Draw a bounding box around every leukocyte (white blood cell).
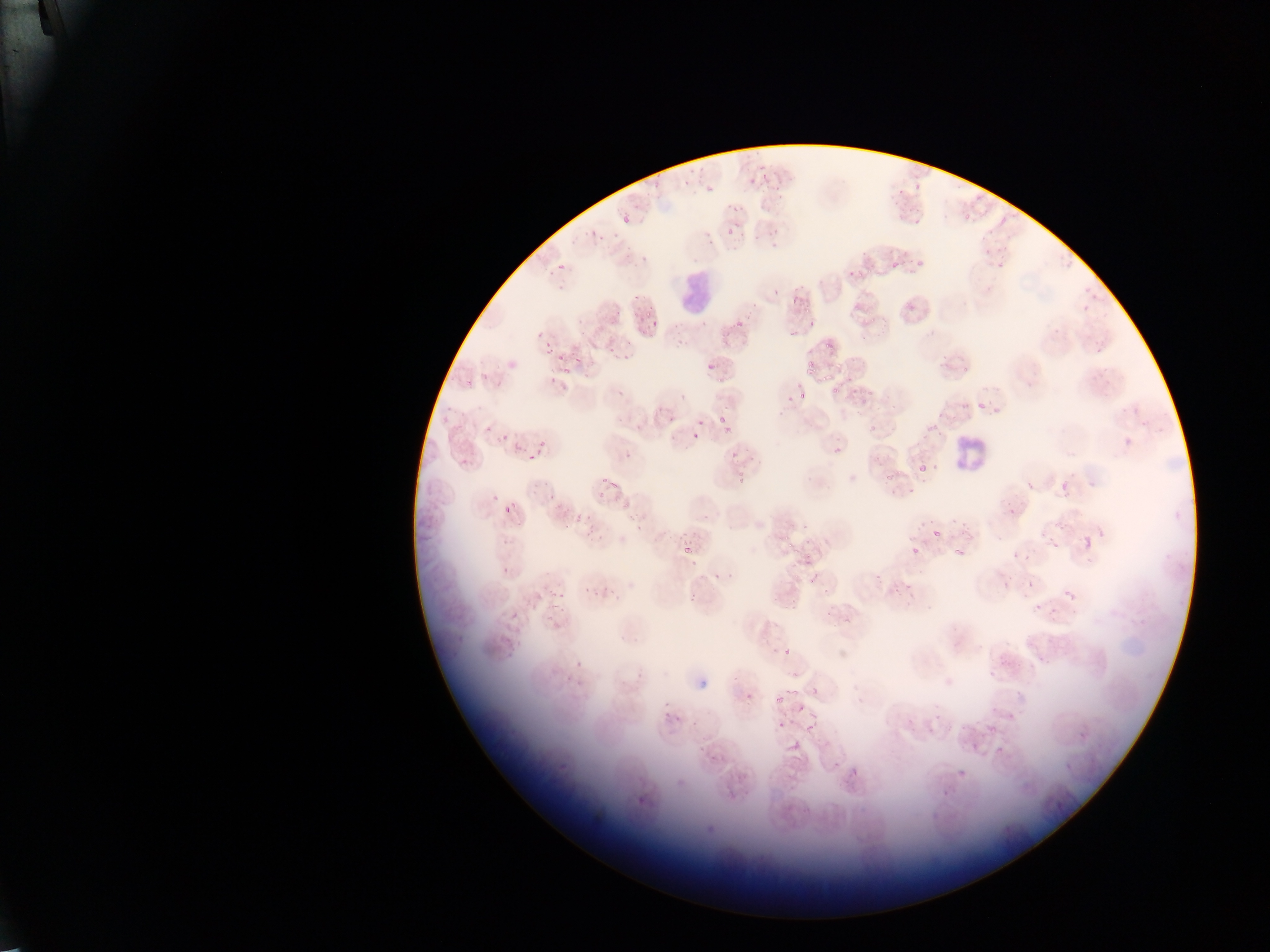

Approximate bounding boxes as [left, top, right, bottom] in pixels.
Leukocytes: [673, 266, 714, 311], [950, 440, 987, 471].

Plasmodium parasite locations = approximate bounding boxes as [left, top, right, bottom] in pixels: [656, 168, 662, 176], [763, 170, 768, 180], [749, 174, 758, 185], [684, 175, 692, 187], [913, 183, 922, 191], [772, 184, 780, 193], [732, 204, 740, 212], [622, 210, 636, 223], [962, 213, 972, 223], [591, 227, 598, 235], [726, 227, 734, 237], [769, 227, 782, 238], [569, 233, 577, 244], [889, 260, 901, 272], [557, 262, 568, 269], [547, 268, 556, 278], [856, 273, 864, 278], [557, 284, 564, 292], [771, 288, 781, 297], [789, 297, 799, 303], [802, 309, 810, 315], [645, 310, 651, 319], [807, 318, 820, 329], [650, 320, 657, 328], [734, 321, 746, 331], [578, 329, 587, 337], [789, 331, 797, 341], [537, 332, 545, 341], [544, 341, 553, 350], [826, 343, 833, 351], [543, 351, 551, 355], [622, 351, 628, 359], [571, 353, 582, 362], [557, 354, 565, 362], [706, 362, 715, 371], [805, 368, 813, 376], [822, 373, 833, 383], [465, 378, 471, 386], [618, 385, 629, 396], [830, 385, 841, 396], [784, 394, 794, 405], [977, 403, 986, 410], [1120, 409, 1128, 415], [717, 416, 725, 424], [1142, 420, 1148, 428], [483, 423, 494, 435], [870, 423, 878, 432], [723, 424, 732, 435], [501, 434, 512, 445], [692, 434, 698, 442], [1122, 435, 1133, 443], [536, 444, 544, 452], [623, 447, 631, 462], [730, 448, 741, 459], [526, 453, 535, 459], [460, 456, 472, 469], [934, 462, 938, 473], [919, 464, 929, 474], [601, 472, 609, 485], [737, 472, 745, 483], [884, 472, 894, 480], [607, 480, 619, 490], [1059, 480, 1069, 491], [1084, 481, 1092, 489], [1025, 482, 1032, 490], [908, 487, 916, 494], [546, 492, 554, 500], [593, 494, 603, 501], [511, 500, 517, 508], [622, 500, 632, 510], [502, 506, 510, 514], [1007, 507, 1015, 515], [703, 510, 711, 522], [574, 514, 581, 522], [949, 516, 957, 523], [927, 517, 937, 525], [961, 519, 969, 526], [634, 525, 643, 532], [960, 527, 968, 535], [932, 529, 941, 539], [584, 530, 595, 539], [675, 532, 687, 539], [995, 534, 1003, 541], [1079, 535, 1096, 555], [1049, 538, 1062, 552], [786, 539, 793, 550], [682, 542, 694, 554], [952, 545, 968, 562], [910, 546, 920, 556], [689, 559, 699, 567], [502, 562, 514, 575], [713, 570, 721, 584], [726, 572, 734, 580], [808, 574, 820, 586], [903, 580, 916, 588], [1026, 580, 1035, 590], [603, 584, 608, 592], [584, 586, 590, 594], [1062, 587, 1078, 604], [551, 589, 557, 599], [555, 592, 564, 601], [688, 592, 695, 602], [547, 599, 558, 610], [557, 608, 568, 618], [511, 611, 521, 621], [505, 635, 513, 642], [782, 647, 794, 656], [574, 663, 581, 671], [988, 668, 999, 676], [636, 672, 643, 680], [564, 674, 572, 682], [734, 674, 742, 683], [790, 687, 799, 696], [812, 688, 821, 696], [745, 691, 758, 703], [775, 695, 783, 703], [661, 700, 671, 708], [672, 716, 683, 724], [776, 718, 786, 726], [988, 720, 1000, 731], [803, 722, 813, 730], [970, 741, 978, 750], [699, 744, 708, 753], [993, 744, 1005, 754], [709, 753, 719, 765], [1063, 760, 1076, 774], [957, 763, 971, 776], [938, 788, 950, 796], [1054, 798, 1068, 814] | approximate [x, y] pixel centers of objects too small to bound: [654, 185], [584, 236], [756, 238], [601, 239], [635, 296], [618, 311], [637, 316], [610, 320], [611, 348], [810, 363], [566, 371], [965, 371], [720, 379], [869, 393], [802, 395], [790, 398], [862, 401], [699, 423], [934, 427], [494, 496], [589, 517], [631, 519], [791, 525], [590, 526], [918, 527], [797, 552], [877, 577], [596, 593], [1037, 607], [1052, 611], [801, 708], [666, 715], [694, 723]
image size = 1270×952 pixels
field of view = single
capture = mobile-phone photograph through a microscope
preparation = thin blood smear
country = Ghana